Give the position of each P. falciparum parasite with its life-cycle stage, each leukocyte, and any debris.
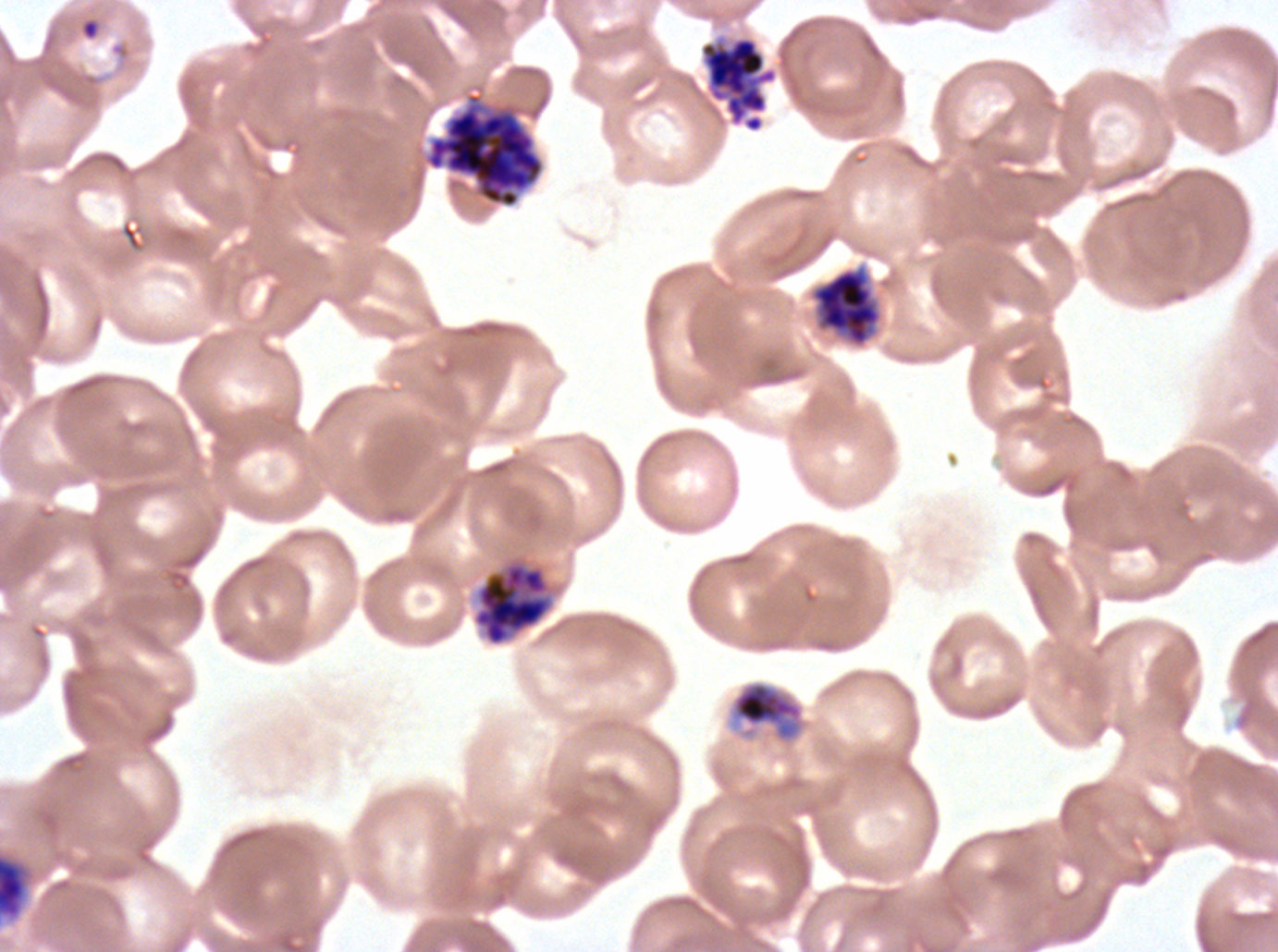

Approximate bounding rectangles given as corner coordinates in pixels from the top-left.
Rings: (x1=80, y1=18, x2=100, y2=41).
Mid trophozoites: (x1=728, y1=679, x2=808, y2=746).
Late schizonts: (x1=425, y1=92, x2=545, y2=208), (x1=811, y1=268, x2=881, y2=347), (x1=473, y1=561, x2=552, y2=646).
Segmenters: (x1=698, y1=33, x2=779, y2=134), (x1=0, y1=851, x2=33, y2=922).
No late-ring/early-trophozoite forms, late trophozoites, early schizonts, gametocytes, leukocytes, or debris observed.

specimen = P. falciparum from a patient in The Gambia, cultured ex vivo for 24 to 48 hours
life-cycle stages observed = ring, mid trophozoite, late schizont, segmenter
image size = 1278×952 pixels
stain = Giemsa
preparation = thin blood smear
field of view = one sub-image of a larger composite